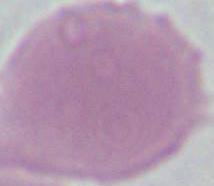

identification = red blood cell
magnification = 1000x
modality = photomicrograph